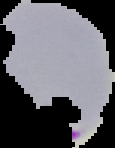
Summary:
  - Image type: cell region segmented out of the field of view; surrounding area masked to black
  - Malaria status: parasitized
  - Image size: 115×148 pixels
  - Preparation: thin blood film